Locate and identify every blood parasite.
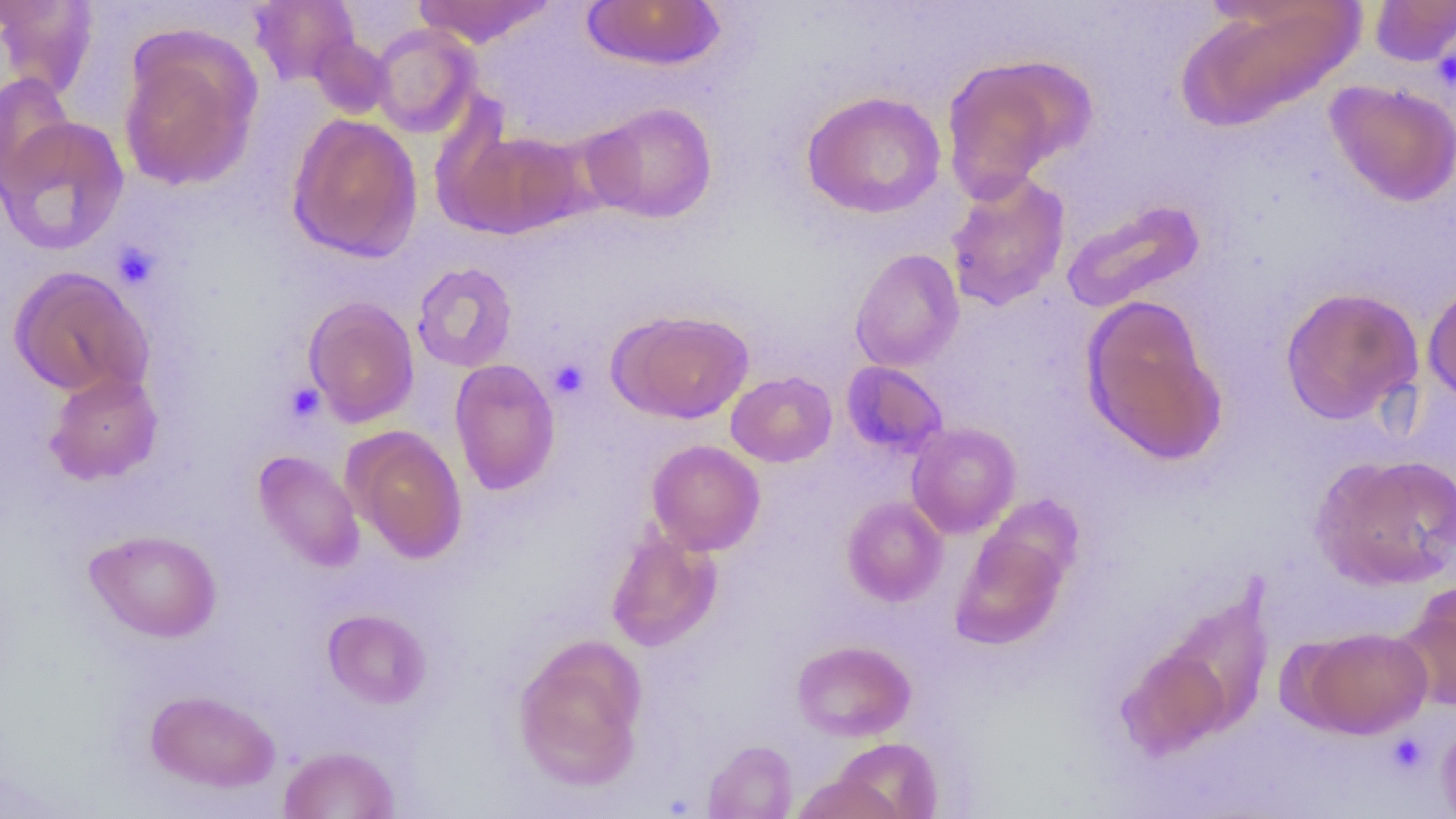
No blood parasites observed.

Approximate bounding boxes as named x1/y1/x2/y2 corners in pixels. Platelet locations: (x1=1432, y1=36, x2=1456, y2=97), (x1=112, y1=240, x2=161, y2=290), (x1=549, y1=359, x2=588, y2=399), (x1=284, y1=382, x2=326, y2=424), (x1=1386, y1=732, x2=1429, y2=776). Uninfected red blood cell locations: (x1=0, y1=0, x2=99, y2=100), (x1=248, y1=0, x2=359, y2=87), (x1=413, y1=0, x2=556, y2=47), (x1=582, y1=0, x2=724, y2=71), (x1=1369, y1=0, x2=1456, y2=66), (x1=1179, y1=2, x2=1363, y2=130), (x1=370, y1=23, x2=481, y2=138), (x1=118, y1=35, x2=261, y2=192), (x1=310, y1=36, x2=392, y2=119), (x1=940, y1=55, x2=1087, y2=199), (x1=0, y1=73, x2=76, y2=196), (x1=1325, y1=79, x2=1456, y2=206), (x1=801, y1=90, x2=946, y2=218), (x1=584, y1=101, x2=718, y2=223), (x1=287, y1=113, x2=423, y2=263), (x1=0, y1=116, x2=129, y2=256), (x1=442, y1=126, x2=589, y2=239), (x1=944, y1=170, x2=1071, y2=311), (x1=1061, y1=199, x2=1206, y2=313), (x1=850, y1=248, x2=964, y2=372), (x1=411, y1=262, x2=518, y2=373), (x1=8, y1=265, x2=154, y2=400), (x1=1422, y1=280, x2=1456, y2=407), (x1=1279, y1=286, x2=1423, y2=425), (x1=1080, y1=294, x2=1227, y2=466), (x1=303, y1=297, x2=420, y2=427), (x1=610, y1=309, x2=755, y2=424), (x1=448, y1=358, x2=561, y2=496), (x1=841, y1=361, x2=948, y2=458), (x1=44, y1=369, x2=163, y2=485), (x1=725, y1=371, x2=837, y2=467), (x1=906, y1=422, x2=1021, y2=538), (x1=346, y1=426, x2=468, y2=564), (x1=647, y1=439, x2=765, y2=555), (x1=252, y1=450, x2=365, y2=572), (x1=1312, y1=453, x2=1456, y2=590), (x1=981, y1=494, x2=1085, y2=593), (x1=842, y1=497, x2=948, y2=606), (x1=84, y1=528, x2=222, y2=642), (x1=605, y1=528, x2=722, y2=652), (x1=950, y1=528, x2=1068, y2=650), (x1=1395, y1=584, x2=1456, y2=712), (x1=322, y1=608, x2=432, y2=709), (x1=1298, y1=626, x2=1432, y2=738), (x1=512, y1=634, x2=648, y2=791), (x1=791, y1=639, x2=916, y2=741), (x1=1118, y1=645, x2=1232, y2=760), (x1=145, y1=689, x2=280, y2=793), (x1=1436, y1=715, x2=1456, y2=815), (x1=831, y1=737, x2=943, y2=819), (x1=702, y1=739, x2=798, y2=818), (x1=278, y1=745, x2=400, y2=818), (x1=790, y1=773, x2=905, y2=818). Slide-level diagnosis: negative for blood parasites. Image is 1456×819 pixels. 1000x magnification. Light microscopy. Thin blood smear. Single field of view.